Comment on the morphology of the erythrocytes.
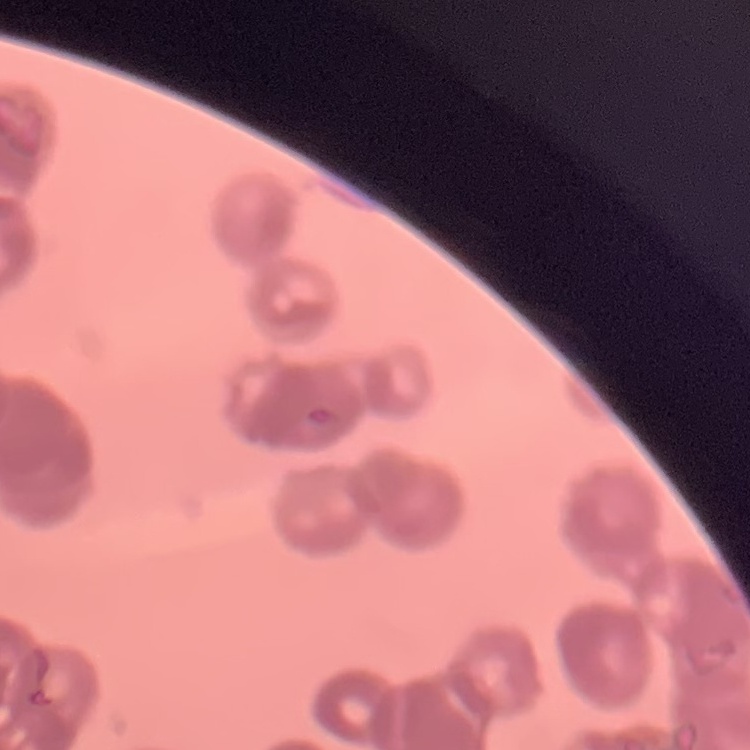
They show rouleaux formation.

Stained with either Field's or Giemsa. Thin peripheral smear. Square crop of a larger photomicrograph.